Assess for malaria.
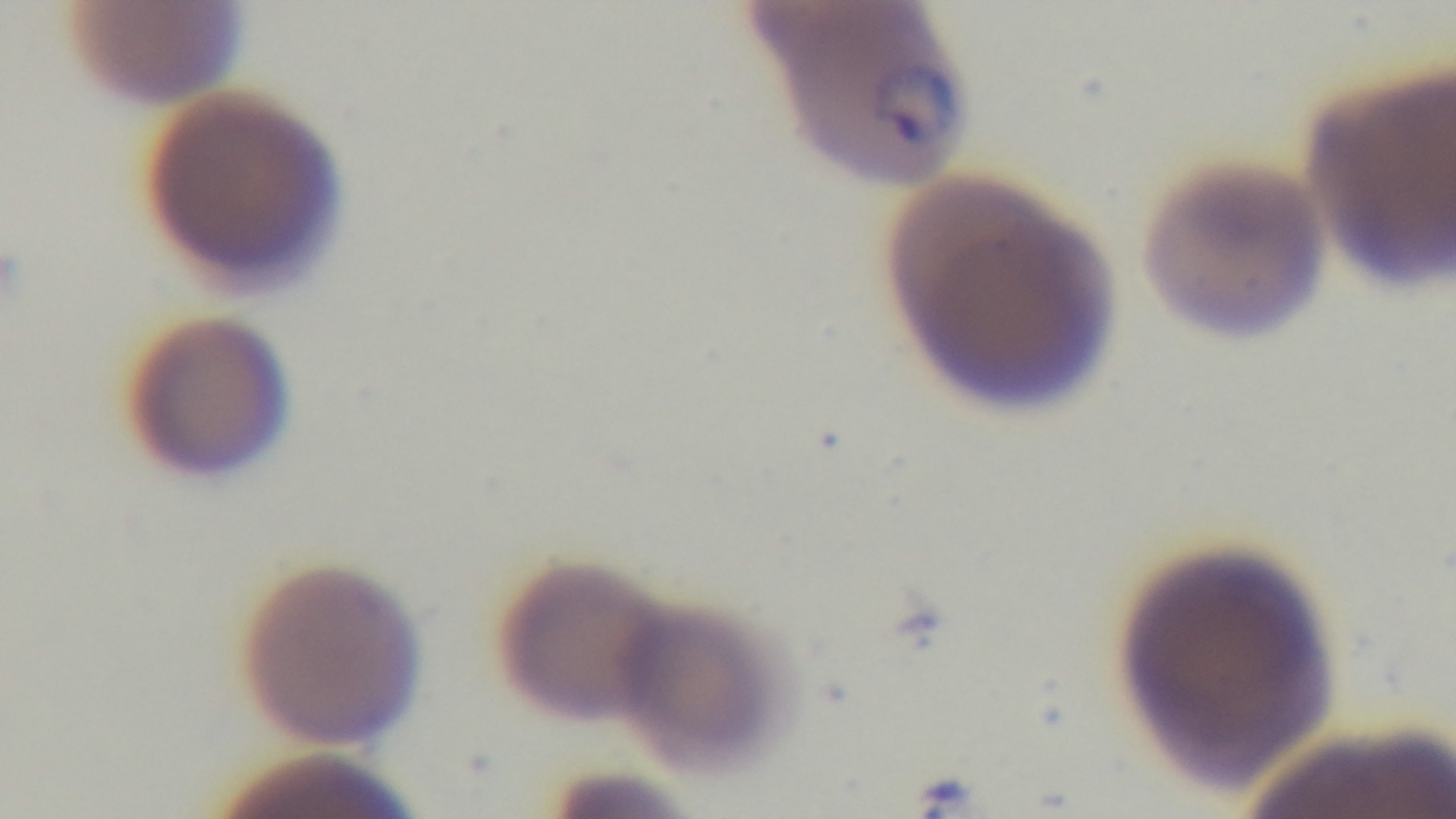

It is infected.

Oil-immersion objective, 100x. Captured with a mounted 4K digital camera. One field from the slide. Photomicrograph. Preparation: thin blood film. Giemsa stain.